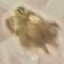

Result: no malaria parasites seen. Thin blood smear. Giemsa stain. Acquired by smartphone through the microscope eyepiece. Automatically extracted cell patch, resized to 64 × 64 pixels.